Outline each uninfected red blood cell.
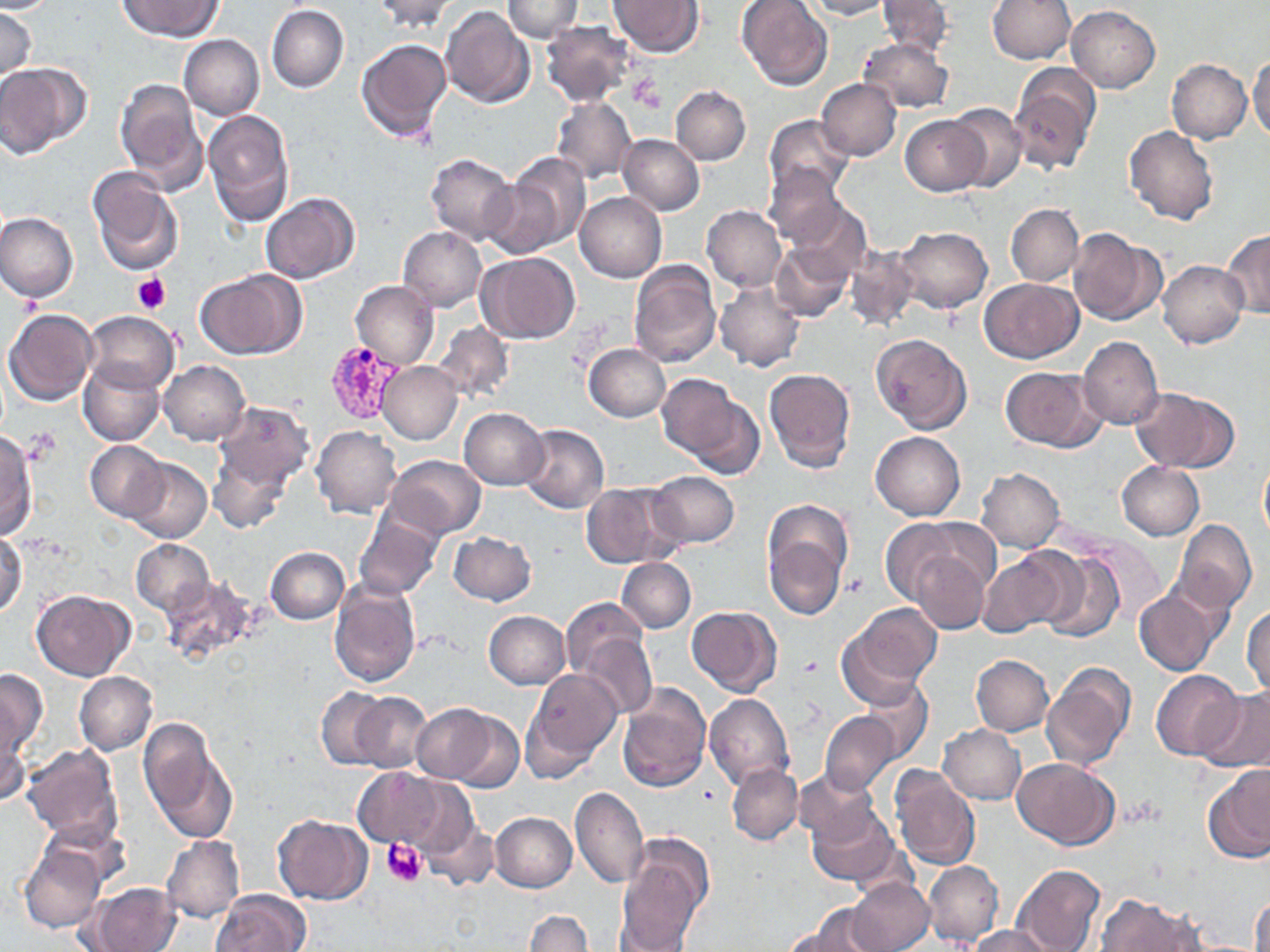

Approximate bounding boxes as named x1/y1/x2/y2 corners in pixels.
Uninfected red blood cells: (x1=0, y1=0, x2=58, y2=13), (x1=118, y1=0, x2=222, y2=41), (x1=371, y1=0, x2=460, y2=33), (x1=502, y1=0, x2=583, y2=41), (x1=738, y1=0, x2=832, y2=90), (x1=804, y1=0, x2=892, y2=20), (x1=877, y1=0, x2=953, y2=58), (x1=988, y1=0, x2=1075, y2=64), (x1=611, y1=1, x2=704, y2=56), (x1=267, y1=5, x2=349, y2=94), (x1=1067, y1=5, x2=1160, y2=92), (x1=440, y1=6, x2=534, y2=108), (x1=0, y1=8, x2=37, y2=81), (x1=540, y1=21, x2=635, y2=106), (x1=179, y1=34, x2=264, y2=119), (x1=859, y1=36, x2=954, y2=112), (x1=356, y1=38, x2=451, y2=142), (x1=1249, y1=50, x2=1270, y2=144), (x1=1167, y1=58, x2=1253, y2=143), (x1=0, y1=62, x2=88, y2=158), (x1=1009, y1=64, x2=1101, y2=175), (x1=816, y1=78, x2=902, y2=160), (x1=114, y1=79, x2=208, y2=194), (x1=671, y1=84, x2=750, y2=164), (x1=551, y1=96, x2=637, y2=184), (x1=945, y1=102, x2=1028, y2=192), (x1=203, y1=109, x2=296, y2=226), (x1=765, y1=115, x2=855, y2=198), (x1=900, y1=115, x2=988, y2=195), (x1=1124, y1=126, x2=1218, y2=226), (x1=617, y1=134, x2=704, y2=215), (x1=425, y1=153, x2=518, y2=244), (x1=494, y1=153, x2=590, y2=255), (x1=762, y1=162, x2=847, y2=248), (x1=86, y1=166, x2=185, y2=278), (x1=260, y1=192, x2=359, y2=283), (x1=575, y1=192, x2=666, y2=282), (x1=787, y1=201, x2=871, y2=279), (x1=1005, y1=203, x2=1083, y2=286), (x1=701, y1=206, x2=786, y2=292), (x1=0, y1=211, x2=78, y2=304), (x1=397, y1=226, x2=486, y2=311), (x1=894, y1=226, x2=992, y2=313), (x1=1069, y1=229, x2=1166, y2=326), (x1=1223, y1=231, x2=1270, y2=317), (x1=771, y1=243, x2=855, y2=322), (x1=843, y1=247, x2=918, y2=331), (x1=478, y1=252, x2=581, y2=343), (x1=1158, y1=260, x2=1248, y2=347), (x1=629, y1=261, x2=721, y2=367), (x1=195, y1=269, x2=303, y2=360), (x1=980, y1=278, x2=1082, y2=363), (x1=351, y1=280, x2=438, y2=368), (x1=713, y1=281, x2=804, y2=371), (x1=3, y1=309, x2=97, y2=407), (x1=83, y1=310, x2=178, y2=395), (x1=434, y1=322, x2=515, y2=404), (x1=870, y1=333, x2=972, y2=433), (x1=1078, y1=336, x2=1163, y2=431), (x1=583, y1=344, x2=671, y2=422), (x1=158, y1=360, x2=249, y2=446), (x1=377, y1=361, x2=464, y2=444), (x1=79, y1=362, x2=165, y2=446), (x1=1000, y1=367, x2=1104, y2=452), (x1=763, y1=368, x2=857, y2=473), (x1=657, y1=372, x2=743, y2=463), (x1=1131, y1=387, x2=1239, y2=472), (x1=681, y1=397, x2=765, y2=479), (x1=212, y1=402, x2=314, y2=495), (x1=459, y1=407, x2=550, y2=490), (x1=519, y1=424, x2=609, y2=513), (x1=311, y1=426, x2=402, y2=518), (x1=0, y1=431, x2=39, y2=539), (x1=870, y1=431, x2=965, y2=520), (x1=85, y1=441, x2=170, y2=521), (x1=209, y1=446, x2=293, y2=534), (x1=385, y1=455, x2=486, y2=540), (x1=1258, y1=455, x2=1270, y2=544), (x1=125, y1=458, x2=211, y2=543), (x1=1116, y1=461, x2=1205, y2=540), (x1=977, y1=468, x2=1065, y2=553), (x1=646, y1=471, x2=740, y2=549), (x1=581, y1=480, x2=683, y2=568), (x1=354, y1=511, x2=443, y2=599), (x1=879, y1=517, x2=968, y2=605), (x1=1172, y1=519, x2=1257, y2=614), (x1=762, y1=521, x2=848, y2=623), (x1=0, y1=530, x2=26, y2=620), (x1=448, y1=531, x2=537, y2=606), (x1=1088, y1=537, x2=1165, y2=621), (x1=130, y1=539, x2=214, y2=615), (x1=264, y1=546, x2=348, y2=624), (x1=977, y1=549, x2=1073, y2=636), (x1=1038, y1=549, x2=1125, y2=643), (x1=911, y1=550, x2=991, y2=634), (x1=616, y1=557, x2=695, y2=633), (x1=160, y1=575, x2=262, y2=662), (x1=328, y1=578, x2=420, y2=686), (x1=1133, y1=584, x2=1226, y2=676), (x1=31, y1=589, x2=134, y2=680), (x1=560, y1=597, x2=652, y2=682), (x1=1243, y1=603, x2=1270, y2=697), (x1=841, y1=604, x2=942, y2=698), (x1=687, y1=606, x2=781, y2=696), (x1=484, y1=610, x2=571, y2=689), (x1=577, y1=631, x2=657, y2=718), (x1=970, y1=655, x2=1053, y2=735), (x1=1042, y1=663, x2=1135, y2=773), (x1=525, y1=666, x2=624, y2=768), (x1=0, y1=669, x2=49, y2=763), (x1=1151, y1=669, x2=1246, y2=760), (x1=74, y1=671, x2=157, y2=755), (x1=859, y1=680, x2=933, y2=763), (x1=616, y1=683, x2=710, y2=793), (x1=316, y1=687, x2=390, y2=769), (x1=1199, y1=688, x2=1270, y2=773), (x1=351, y1=692, x2=433, y2=773), (x1=704, y1=693, x2=794, y2=789), (x1=411, y1=703, x2=500, y2=783), (x1=446, y1=709, x2=523, y2=792), (x1=820, y1=710, x2=899, y2=794), (x1=139, y1=718, x2=237, y2=842), (x1=938, y1=724, x2=1025, y2=804), (x1=0, y1=726, x2=29, y2=807), (x1=20, y1=745, x2=124, y2=847), (x1=1013, y1=758, x2=1119, y2=850), (x1=726, y1=763, x2=804, y2=844), (x1=1203, y1=764, x2=1270, y2=863), (x1=890, y1=766, x2=981, y2=871), (x1=353, y1=767, x2=450, y2=850), (x1=794, y1=769, x2=879, y2=848), (x1=397, y1=777, x2=488, y2=867), (x1=569, y1=786, x2=649, y2=889), (x1=808, y1=804, x2=899, y2=885), (x1=490, y1=812, x2=577, y2=892), (x1=273, y1=815, x2=373, y2=905), (x1=421, y1=821, x2=498, y2=891), (x1=160, y1=834, x2=244, y2=924), (x1=19, y1=843, x2=108, y2=933), (x1=617, y1=846, x2=709, y2=952), (x1=923, y1=860, x2=1004, y2=947), (x1=1011, y1=864, x2=1105, y2=952), (x1=848, y1=877, x2=934, y2=952), (x1=83, y1=882, x2=181, y2=952), (x1=211, y1=888, x2=313, y2=952), (x1=1251, y1=892, x2=1270, y2=952), (x1=1095, y1=894, x2=1203, y2=951), (x1=615, y1=898, x2=697, y2=949), (x1=792, y1=906, x2=886, y2=952), (x1=525, y1=910, x2=593, y2=952), (x1=967, y1=926, x2=1059, y2=952), (x1=779, y1=928, x2=866, y2=952).

slide-level diagnosis = Plasmodium vivax
platelet locations = approximate bounding boxes as named x1/y1/x2/y2 corners in pixels: (x1=630, y1=75, x2=664, y2=113), (x1=132, y1=273, x2=171, y2=313), (x1=844, y1=572, x2=869, y2=597), (x1=798, y1=656, x2=825, y2=680), (x1=382, y1=837, x2=428, y2=887)
stain = May-Grünwald-Giemsa
Plasmodium vivax-infected red blood cell locations = approximate bounding boxes as named x1/y1/x2/y2 corners in pixels: (x1=322, y1=340, x2=402, y2=425)
modality = optical microscopy
preparation = thin blood smear
field of view = one of a larger specimen
image size = 1270×952 pixels
magnification = 1000x